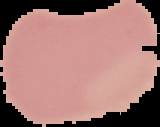
preparation = thin blood film
image type = segmented cell region with the area outside set to black
image size = 160×127 pixels
result = no malaria parasites seen